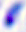 400x magnification. Toxoplasma gondii is shown. Photomicrograph.